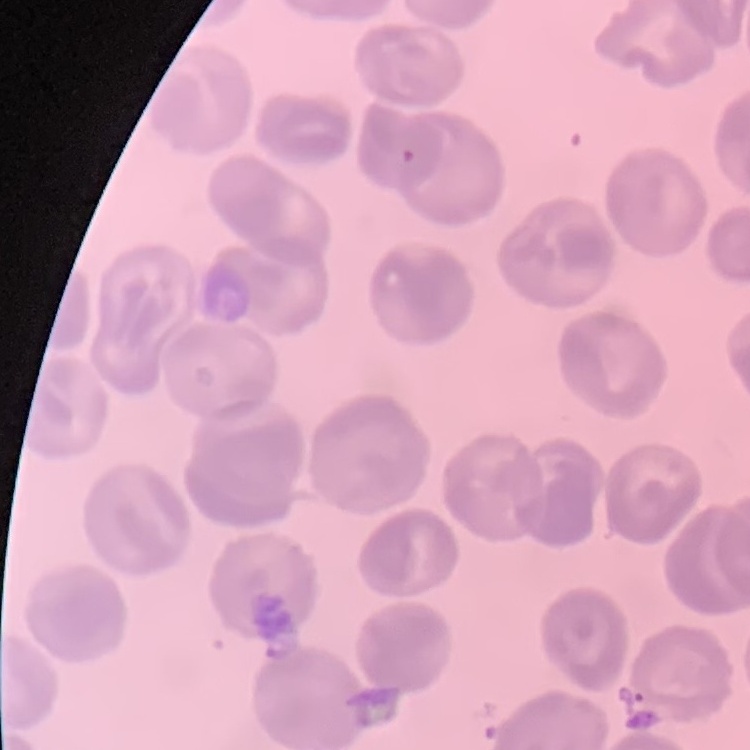

Summary:
  - Red blood cell morphology: no rouleaux formation
  - Image type: one tile cut from a larger photomicrograph
  - Stain: Field's or Giemsa
  - Preparation: thin peripheral smear